Describe the morphology of the erythrocytes.
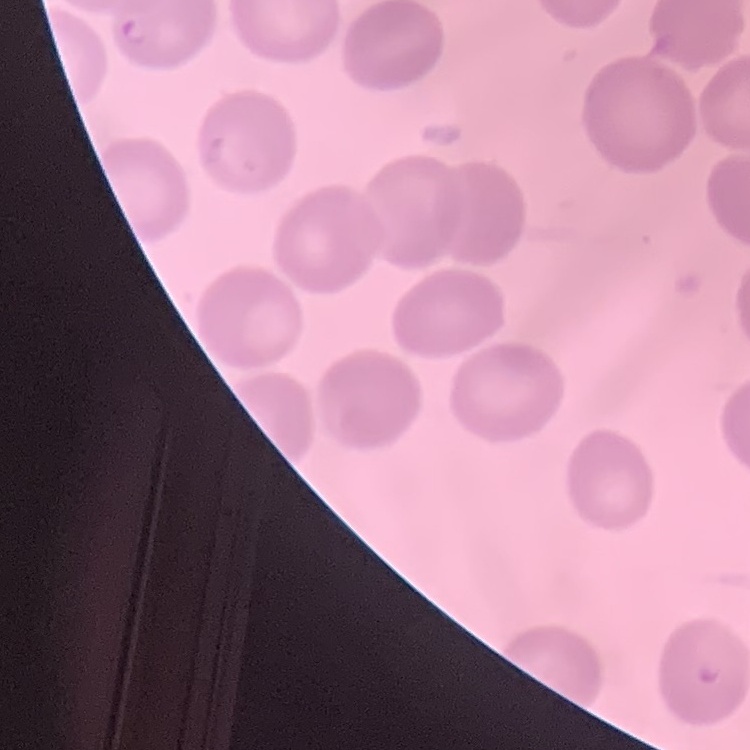

No rouleaux formation.

stain = Field's or Giemsa
preparation = thin peripheral smear
image type = square crop of a larger photomicrograph